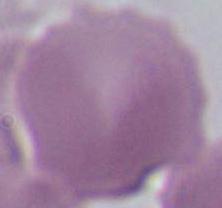
magnification: 1000x
identification: red blood cell
modality: photomicrograph